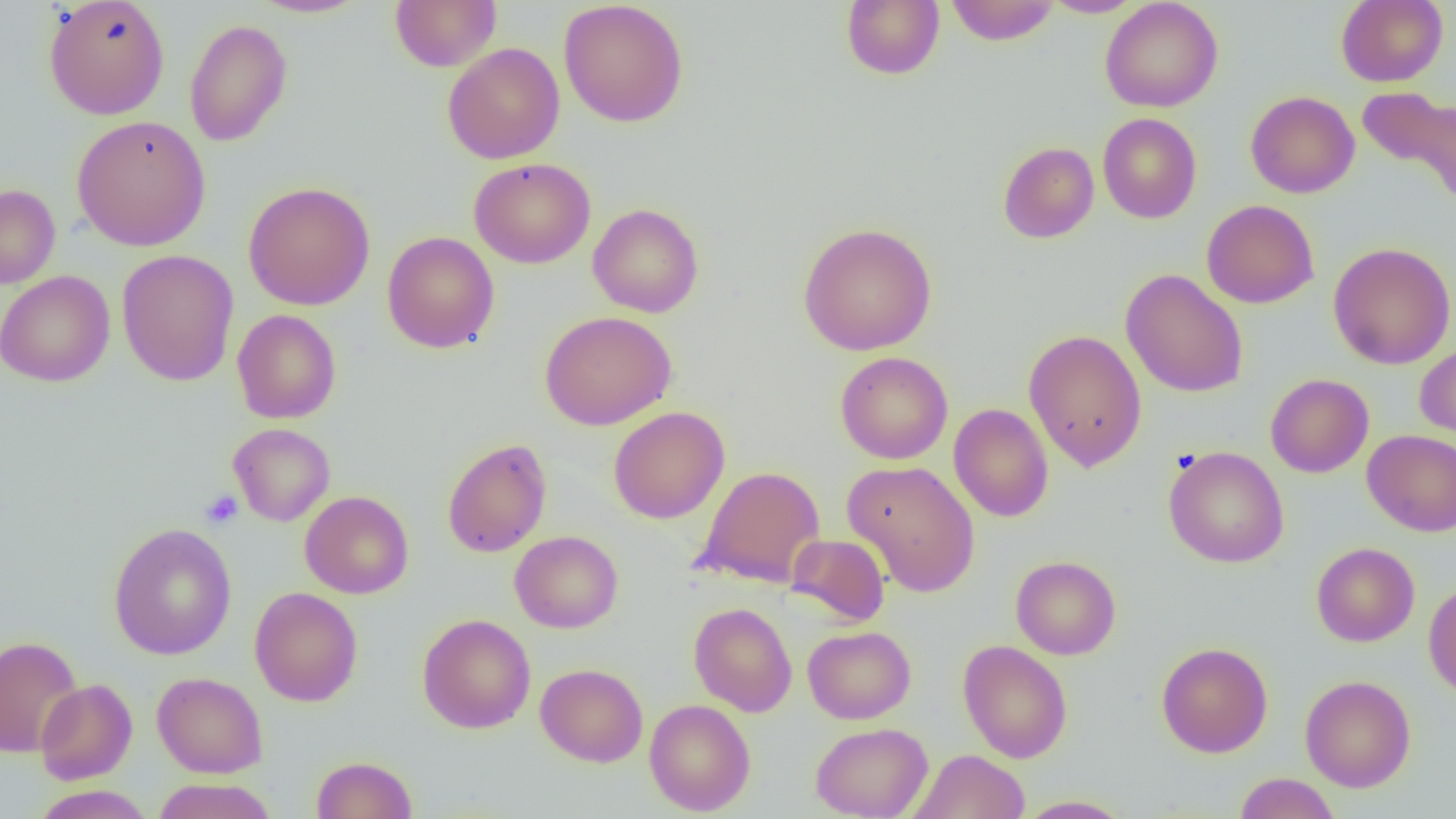
slide-level diagnosis = no evidence of blood parasites
uninfected red blood cell locations = approximate bounding boxes as named x1/y1/x2/y2 corners in pixels: (x1=44, y1=0, x2=170, y2=119), (x1=248, y1=0, x2=370, y2=18), (x1=390, y1=0, x2=502, y2=73), (x1=558, y1=0, x2=689, y2=127), (x1=841, y1=0, x2=944, y2=80), (x1=1039, y1=0, x2=1146, y2=18), (x1=1099, y1=0, x2=1223, y2=112), (x1=1335, y1=0, x2=1448, y2=87), (x1=945, y1=1, x2=1059, y2=45), (x1=184, y1=18, x2=293, y2=147), (x1=442, y1=43, x2=565, y2=164), (x1=1357, y1=85, x2=1456, y2=210), (x1=1245, y1=91, x2=1359, y2=198), (x1=1098, y1=113, x2=1202, y2=223), (x1=71, y1=115, x2=211, y2=252), (x1=998, y1=141, x2=1099, y2=243), (x1=469, y1=158, x2=596, y2=269), (x1=243, y1=181, x2=375, y2=310), (x1=0, y1=184, x2=61, y2=289), (x1=1201, y1=199, x2=1320, y2=308), (x1=588, y1=203, x2=704, y2=318), (x1=797, y1=222, x2=937, y2=356), (x1=382, y1=231, x2=500, y2=353), (x1=1328, y1=242, x2=1456, y2=369), (x1=116, y1=249, x2=239, y2=386), (x1=1120, y1=269, x2=1249, y2=398), (x1=0, y1=270, x2=115, y2=387), (x1=232, y1=309, x2=341, y2=424), (x1=540, y1=311, x2=676, y2=430), (x1=1024, y1=329, x2=1147, y2=472), (x1=1415, y1=342, x2=1456, y2=448), (x1=835, y1=351, x2=953, y2=464), (x1=1265, y1=373, x2=1374, y2=478), (x1=949, y1=403, x2=1054, y2=522), (x1=608, y1=406, x2=729, y2=523), (x1=228, y1=423, x2=336, y2=526), (x1=1362, y1=430, x2=1456, y2=536), (x1=441, y1=437, x2=552, y2=558), (x1=1164, y1=445, x2=1290, y2=568), (x1=843, y1=460, x2=981, y2=597), (x1=695, y1=465, x2=826, y2=588), (x1=300, y1=491, x2=414, y2=598), (x1=108, y1=523, x2=236, y2=660), (x1=510, y1=530, x2=623, y2=633), (x1=787, y1=533, x2=890, y2=626), (x1=1311, y1=542, x2=1420, y2=646), (x1=1010, y1=555, x2=1121, y2=660), (x1=1423, y1=581, x2=1456, y2=699), (x1=249, y1=587, x2=363, y2=706), (x1=689, y1=602, x2=797, y2=717), (x1=416, y1=613, x2=536, y2=733), (x1=803, y1=625, x2=916, y2=724), (x1=0, y1=635, x2=83, y2=758), (x1=958, y1=640, x2=1073, y2=763), (x1=1157, y1=642, x2=1273, y2=758), (x1=535, y1=663, x2=648, y2=767), (x1=152, y1=672, x2=268, y2=778), (x1=1300, y1=675, x2=1416, y2=792), (x1=35, y1=678, x2=137, y2=784), (x1=644, y1=699, x2=756, y2=815), (x1=810, y1=722, x2=933, y2=819), (x1=909, y1=750, x2=1030, y2=819), (x1=311, y1=755, x2=418, y2=818), (x1=1234, y1=773, x2=1340, y2=819), (x1=152, y1=778, x2=278, y2=819), (x1=31, y1=786, x2=154, y2=818), (x1=1015, y1=795, x2=1134, y2=818)
magnification = 1000x
image size = 1456×819 pixels
modality = optical microscopy
field of view = one of a larger specimen
platelet locations = approximate bounding boxes as named x1/y1/x2/y2 corners in pixels: (x1=200, y1=489, x2=243, y2=529)
preparation = thin blood smear